Locate and identify every blood parasite.
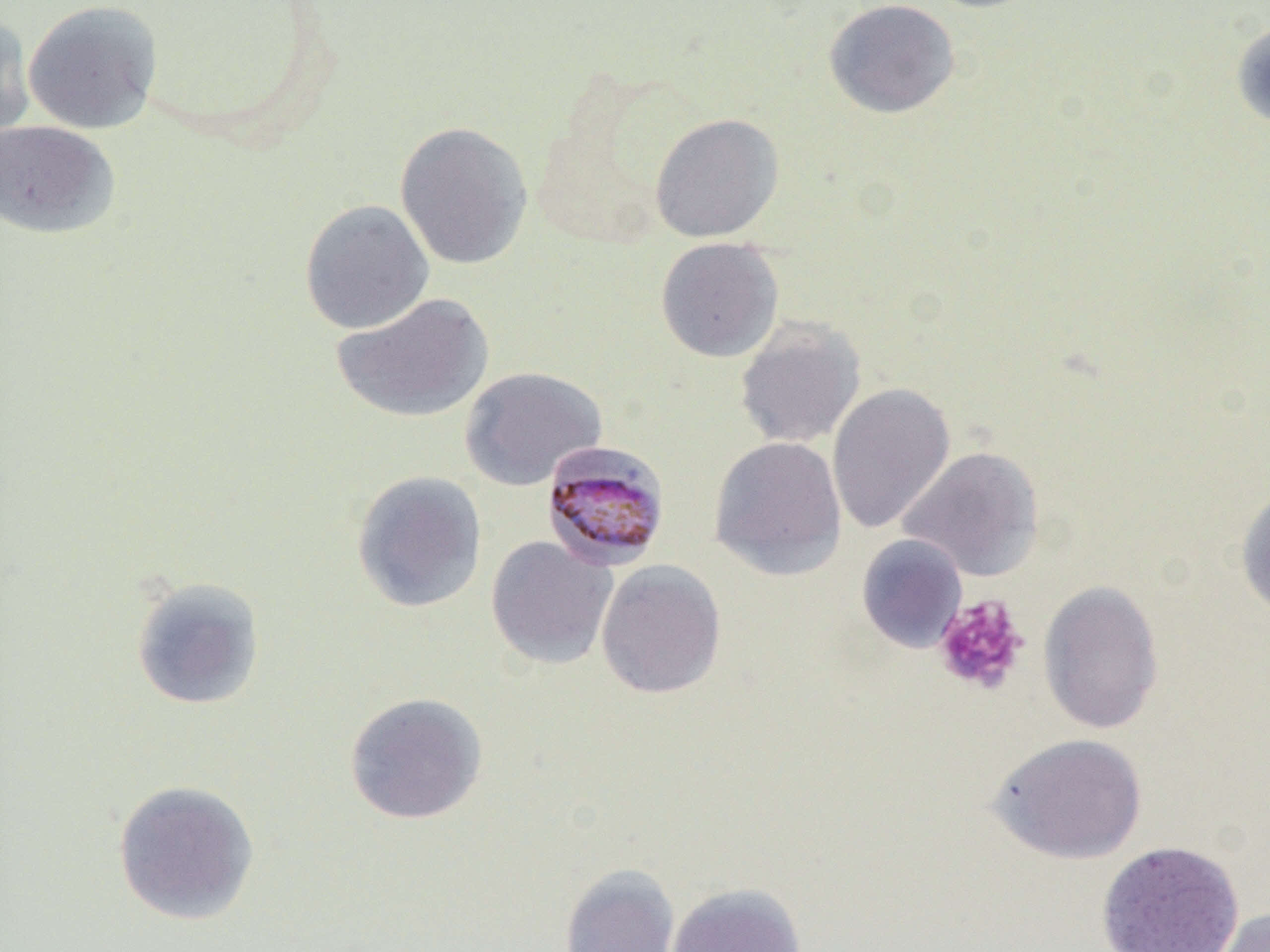

Approximate bounding boxes as named x1/y1/x2/y2 corners in pixels.
Plasmodium malariae-infected red blood cells: (x1=541, y1=440, x2=671, y2=572).
No Plasmodium falciparum, Plasmodium ovale, Plasmodium vivax, Babesia divergens, or Trypanosoma brucei observed.

Summary:
  - Uninfected red blood cell locations: (x1=823, y1=0, x2=961, y2=119), (x1=22, y1=1, x2=163, y2=134), (x1=0, y1=13, x2=36, y2=149), (x1=1231, y1=20, x2=1270, y2=131), (x1=649, y1=113, x2=784, y2=243), (x1=0, y1=120, x2=120, y2=239), (x1=394, y1=120, x2=533, y2=270), (x1=299, y1=199, x2=435, y2=335), (x1=655, y1=237, x2=784, y2=363), (x1=331, y1=292, x2=494, y2=424), (x1=733, y1=319, x2=866, y2=449), (x1=459, y1=367, x2=607, y2=491), (x1=826, y1=383, x2=956, y2=535), (x1=709, y1=436, x2=847, y2=580), (x1=899, y1=446, x2=1044, y2=581), (x1=351, y1=470, x2=487, y2=613), (x1=1235, y1=483, x2=1270, y2=623), (x1=856, y1=534, x2=968, y2=652), (x1=485, y1=535, x2=618, y2=670), (x1=595, y1=559, x2=726, y2=700), (x1=130, y1=576, x2=266, y2=711), (x1=1037, y1=579, x2=1164, y2=735), (x1=344, y1=691, x2=488, y2=825), (x1=989, y1=733, x2=1147, y2=864), (x1=111, y1=779, x2=260, y2=926), (x1=1096, y1=840, x2=1245, y2=952), (x1=559, y1=863, x2=680, y2=952), (x1=665, y1=882, x2=807, y2=952), (x1=1213, y1=906, x2=1270, y2=952)
  - Platelet locations: (x1=932, y1=594, x2=1030, y2=696)
  - Slide-level diagnosis: Plasmodium malariae
  - Magnification: 1000x
  - Modality: optical microscopy
  - Field of view: single
  - Image size: 1270×952 pixels
  - Preparation: thin blood smear